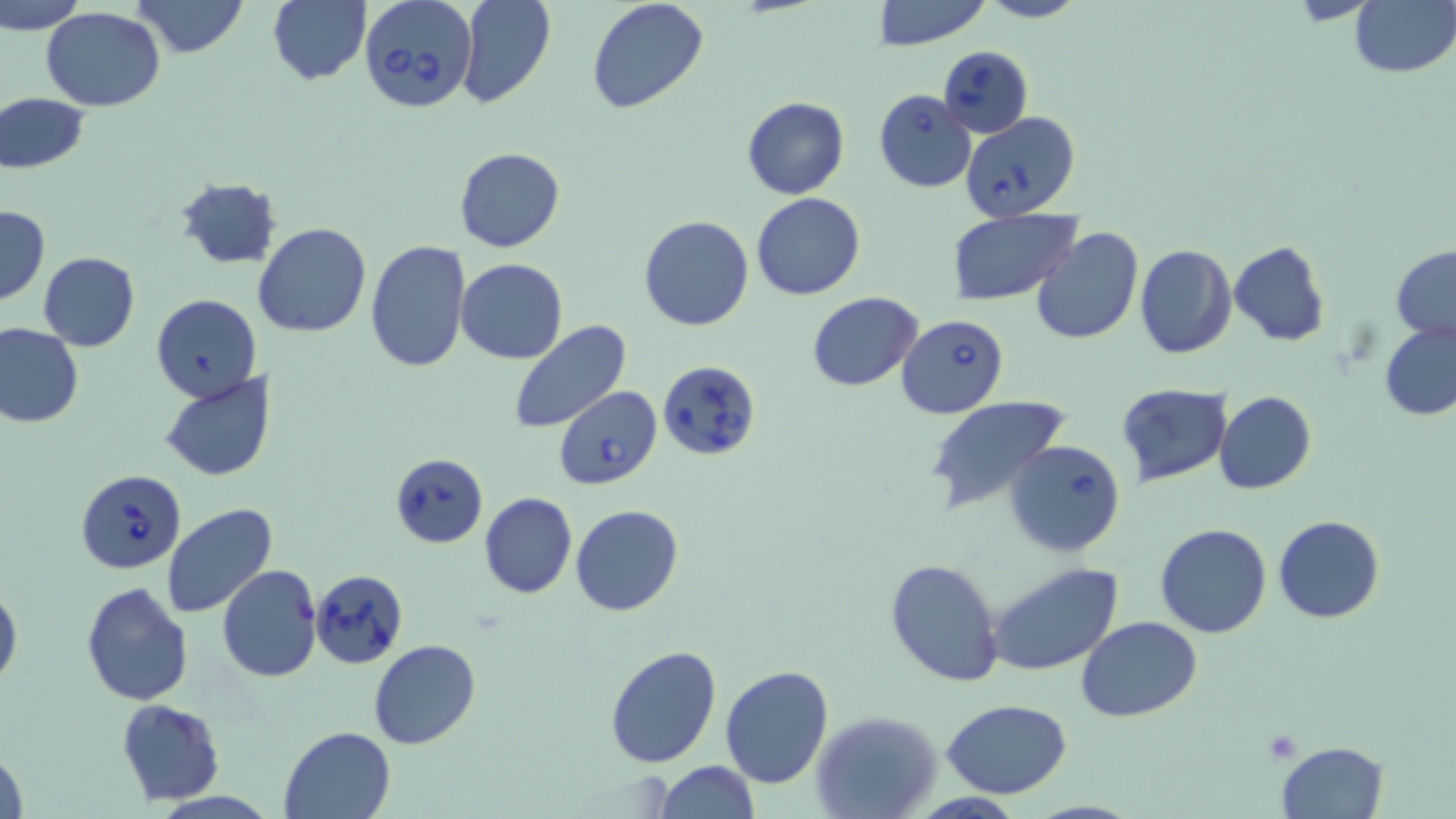

slide-level diagnosis = Babesia divergens
image size = 1456×819 pixels
stain = May-Grünwald-Giemsa
Babesia divergens-infected red blood cell locations = approximate bounding boxes as [x1, y1, x2, y2] in pixels: [358, 0, 479, 115], [937, 45, 1034, 139], [874, 89, 977, 193], [958, 110, 1080, 220], [896, 314, 1008, 418], [658, 359, 760, 461], [553, 386, 662, 489], [1004, 438, 1127, 556], [387, 451, 488, 549], [76, 469, 185, 575], [309, 569, 408, 668]
preparation = thin blood smear
field of view = one of a larger specimen
modality = optical microscopy
magnification = 1000x
uninfected red blood cell locations = approximate bounding boxes as [x1, y1, x2, y2] in pixels: [0, 0, 89, 33], [132, 0, 248, 58], [269, 0, 372, 86], [454, 0, 556, 108], [586, 0, 709, 114], [873, 0, 993, 49], [976, 0, 1087, 24], [1348, 0, 1455, 78], [42, 8, 166, 110], [0, 93, 89, 174], [742, 96, 849, 200], [454, 147, 564, 253], [172, 175, 286, 269], [752, 193, 865, 300], [1, 205, 49, 304], [946, 210, 1079, 306], [639, 214, 754, 331], [254, 223, 371, 338], [1030, 228, 1144, 346], [365, 239, 471, 374], [1229, 242, 1332, 346], [1134, 245, 1237, 359], [1392, 247, 1456, 342], [37, 251, 141, 351], [456, 258, 567, 364], [808, 292, 924, 391], [151, 293, 261, 402], [1380, 319, 1456, 423], [510, 321, 632, 436], [0, 325, 83, 428], [160, 371, 276, 482], [1117, 384, 1232, 486], [1214, 391, 1315, 495], [923, 396, 1070, 518], [478, 492, 578, 599], [162, 503, 278, 620], [571, 505, 684, 617], [1273, 515, 1386, 623], [1156, 523, 1272, 639], [884, 557, 1004, 689], [987, 562, 1126, 679], [216, 566, 322, 682], [81, 580, 194, 704], [0, 584, 23, 692], [1078, 617, 1203, 723], [368, 639, 482, 750], [605, 646, 722, 768], [719, 666, 834, 789], [941, 698, 1071, 798], [117, 699, 225, 804], [811, 711, 941, 819], [278, 725, 398, 818], [1277, 739, 1388, 817], [1, 745, 28, 819], [655, 759, 759, 818]